State which parasite is depicted.
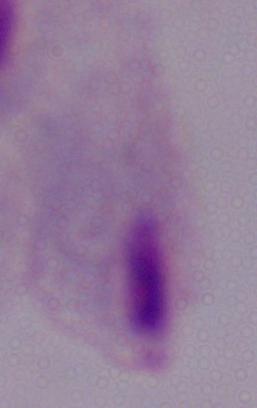

This is a trichomonad.

Summary:
  - Modality: micrograph
  - Magnification: 1000x